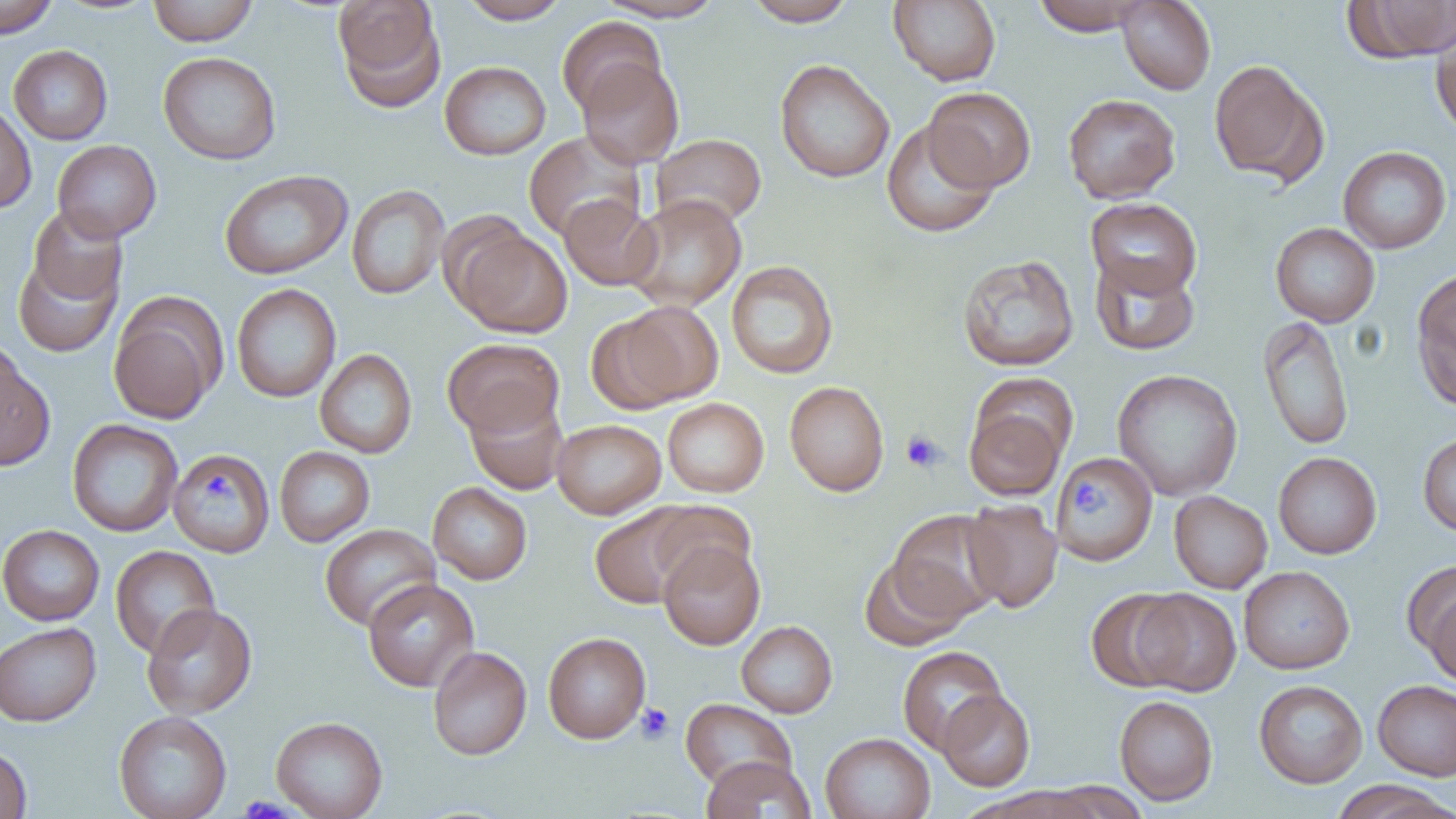

Summary:
  - Coordinate format: approximate bounding boxes as (x1, y1, x2, y2) in pixels
  - Platelet locations: (901, 430, 945, 473), (1067, 481, 1108, 515), (636, 702, 674, 745)
  - Uninfected red blood cell locations: (0, 0, 59, 38), (147, 0, 258, 46), (333, 0, 446, 112), (458, 0, 571, 24), (595, 0, 727, 22), (744, 0, 857, 26), (888, 0, 1001, 86), (1032, 0, 1149, 36), (1116, 0, 1216, 94), (1346, 0, 1456, 62), (557, 16, 666, 116), (1429, 19, 1455, 139), (8, 45, 113, 145), (158, 51, 281, 165), (577, 58, 684, 169), (774, 58, 894, 183), (1209, 59, 1324, 185), (439, 61, 551, 160), (923, 87, 1037, 192), (1063, 93, 1181, 204), (0, 102, 36, 214), (881, 120, 1000, 238), (523, 131, 645, 242), (651, 133, 767, 229), (52, 140, 161, 243), (1338, 146, 1452, 253), (219, 169, 352, 279), (346, 185, 450, 300), (559, 194, 661, 290), (624, 194, 746, 311), (1085, 197, 1202, 299), (26, 205, 128, 308), (1270, 222, 1380, 327), (454, 227, 572, 338), (12, 248, 123, 358), (957, 253, 1080, 372), (1089, 254, 1200, 355), (726, 260, 838, 379), (1412, 271, 1456, 410), (231, 283, 341, 403), (108, 298, 224, 425), (600, 302, 724, 410), (1258, 315, 1354, 451), (443, 338, 564, 438), (0, 347, 55, 471), (315, 349, 417, 458), (1112, 368, 1242, 500), (785, 381, 889, 496), (465, 393, 569, 495), (663, 398, 768, 497), (964, 403, 1068, 501), (66, 419, 183, 537), (552, 419, 666, 519), (1418, 432, 1456, 537), (274, 446, 375, 547), (168, 448, 275, 557), (1273, 452, 1382, 559), (1053, 453, 1158, 566), (428, 482, 532, 585), (1169, 491, 1272, 593), (962, 498, 1063, 612), (645, 500, 756, 592), (589, 505, 703, 609), (887, 510, 1006, 623), (0, 524, 104, 625), (319, 524, 440, 631), (658, 540, 765, 650), (110, 545, 221, 659), (859, 556, 969, 650), (1403, 561, 1455, 669), (1239, 566, 1355, 673), (363, 578, 479, 692), (1424, 587, 1456, 687), (1086, 589, 1191, 692), (1132, 589, 1242, 696), (141, 603, 257, 719), (736, 620, 837, 718), (0, 622, 101, 727), (543, 632, 650, 743), (897, 645, 1007, 755), (428, 646, 532, 760), (1253, 679, 1367, 788), (1372, 679, 1456, 781), (937, 689, 1035, 791), (1114, 695, 1218, 806), (680, 698, 797, 791), (113, 711, 232, 819), (271, 716, 388, 819), (820, 732, 936, 819), (0, 744, 32, 818), (701, 756, 816, 819), (1330, 781, 1454, 819), (1041, 782, 1154, 818)
  - Slide-level diagnosis: negative for blood parasites
  - Image size: 1456×819 pixels
  - Preparation: thin blood film
  - Field of view: single
  - Magnification: 1000x
  - Modality: optical microscopy